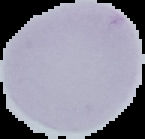 The area outside the segmented cell region is set to black. Image is 145×139 pixels. From a thin blood smear. Malaria status: uninfected.